Identify the blood parasite species.
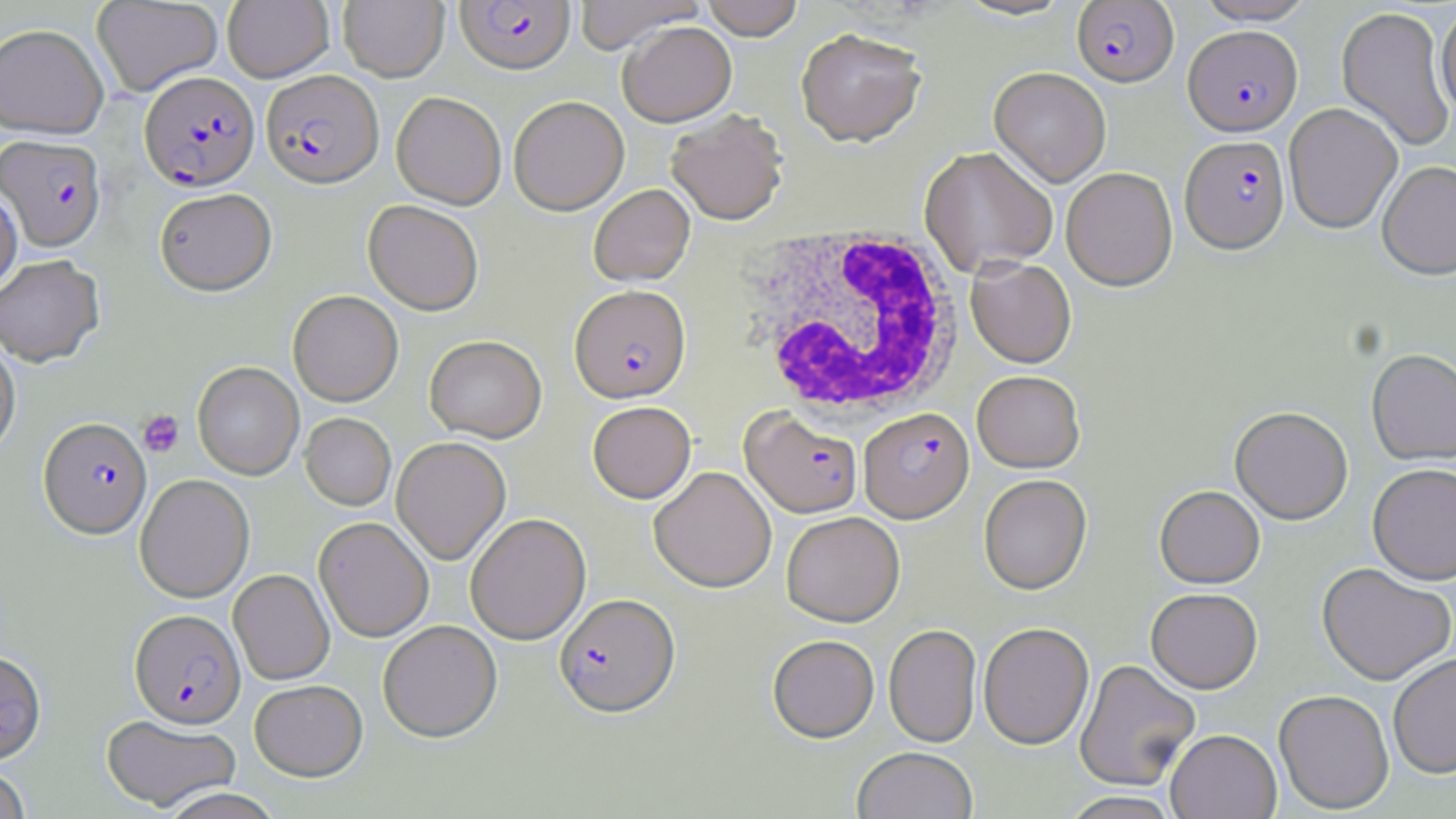
Plasmodium falciparum.

image size = 1456×819 pixels
stain = May-Grünwald-Giemsa
preparation = thin blood smear
uninfected red blood cell locations = approximate bounding boxes as (x1,y1)-(x2,y2) corner pairs in pixels: (92,0)-(223,97), (222,0)-(334,82), (338,0)-(449,81), (574,0)-(706,55), (701,0)-(803,43), (954,0)-(1076,22), (1195,0)-(1317,25), (1335,5)-(1455,153), (1435,5)-(1456,118), (0,23)-(109,139), (619,23)-(737,129), (795,31)-(926,150), (989,68)-(1111,189), (391,92)-(506,209), (509,97)-(629,217), (1283,103)-(1403,235), (666,112)-(788,227), (919,148)-(1058,278), (1377,161)-(1456,282), (1062,168)-(1178,293), (0,183)-(22,296), (589,185)-(695,287), (154,188)-(277,296), (363,201)-(483,316), (0,254)-(104,367), (965,258)-(1077,370), (288,291)-(403,407), (0,335)-(20,458), (424,336)-(546,443), (1366,350)-(1456,466), (192,362)-(304,480), (972,372)-(1085,474), (587,401)-(696,504), (1230,409)-(1354,526), (300,413)-(396,511), (391,437)-(511,565), (1367,465)-(1456,587), (649,466)-(776,593), (135,474)-(254,603), (979,476)-(1092,596), (1154,486)-(1265,590), (781,512)-(905,627), (465,513)-(591,644), (314,517)-(434,642), (1316,565)-(1455,687), (229,570)-(334,685), (1145,589)-(1263,695), (378,621)-(502,742), (978,623)-(1094,750), (883,624)-(982,748), (767,635)-(879,743), (0,650)-(47,764), (1388,654)-(1456,780), (1075,660)-(1201,792), (249,680)-(367,781), (1273,691)-(1394,815), (100,715)-(241,812), (1166,730)-(1281,819), (852,747)-(979,819), (0,766)-(30,819), (158,788)-(284,819), (1059,792)-(1182,819)
magnification = 1000x
Plasmodium falciparum-infected red blood cell locations = approximate bounding boxes as (x1,y1)-(x2,y2) corner pairs in pixels: (456,1)-(575,76), (1072,1)-(1179,87), (1184,25)-(1302,136), (260,70)-(383,188), (140,71)-(260,192), (1,135)-(106,251), (1180,136)-(1290,255), (569,286)-(691,404), (740,408)-(863,519), (859,408)-(974,523), (38,418)-(152,538), (554,594)-(680,718), (130,609)-(246,728)
modality = light microscopy
white blood cell locations = approximate bounding boxes as (x1,y1)-(x2,y2) corner pairs in pixels: (738,224)-(965,422)
field of view = one of a larger specimen
platelet locations = approximate bounding boxes as (x1,y1)-(x2,y2) corner pairs in pixels: (138,410)-(184,458)